State the blood parasite species.
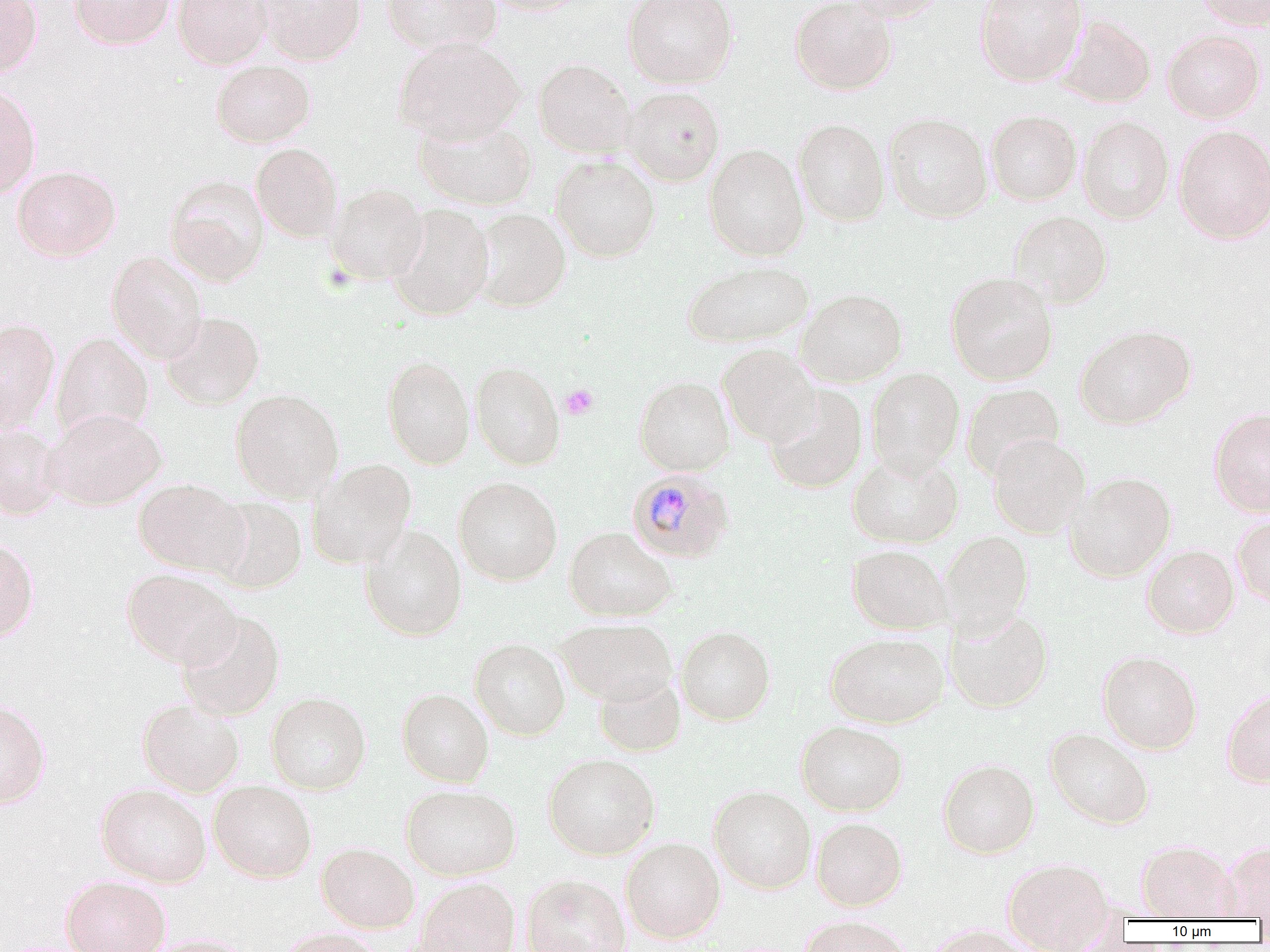
Plasmodium malariae.

Summary:
  - Coordinate format: approximate bounding boxes as [x1, y1, x2, y2] in pixels
  - Plasmodium malariae-infected red blood cell locations: [626, 469, 735, 564]
  - Platelet locations: [560, 384, 599, 419]
  - Uninfected red blood cell locations: [0, 0, 42, 79], [70, 0, 175, 49], [172, 0, 272, 69], [258, 0, 366, 64], [382, 0, 501, 55], [480, 0, 590, 15], [623, 0, 738, 88], [790, 0, 897, 94], [844, 0, 949, 22], [974, 0, 1086, 85], [1195, 0, 1270, 30], [1056, 16, 1156, 107], [1163, 28, 1266, 122], [392, 38, 525, 142], [534, 58, 635, 157], [211, 60, 315, 147], [0, 84, 41, 198], [622, 86, 724, 186], [986, 110, 1082, 205], [884, 112, 992, 223], [1077, 116, 1174, 224], [413, 117, 538, 211], [793, 119, 890, 225], [1173, 125, 1270, 244], [250, 142, 344, 242], [704, 144, 808, 261], [550, 155, 661, 262], [12, 165, 120, 261], [164, 175, 270, 286], [326, 184, 428, 284], [386, 204, 494, 320], [472, 208, 571, 311], [1010, 210, 1112, 307], [107, 250, 207, 363], [682, 260, 814, 348], [946, 273, 1057, 385], [796, 288, 907, 387], [161, 311, 265, 409], [0, 317, 61, 431], [1076, 325, 1196, 428], [51, 332, 154, 439], [718, 344, 820, 446], [382, 354, 475, 469], [470, 360, 566, 470], [866, 367, 964, 477], [634, 375, 734, 475], [962, 383, 1064, 479], [764, 385, 868, 493], [231, 388, 344, 502], [1208, 407, 1270, 516], [45, 408, 166, 510], [0, 424, 65, 520], [988, 433, 1090, 537], [847, 451, 963, 549], [307, 458, 417, 569], [1065, 472, 1176, 581], [453, 477, 563, 586], [134, 479, 248, 575], [208, 496, 307, 594], [1233, 514, 1270, 608], [360, 525, 467, 641], [564, 526, 676, 621], [938, 531, 1033, 637], [0, 538, 40, 643], [847, 544, 952, 634], [1142, 545, 1238, 638], [121, 568, 240, 669], [945, 607, 1053, 713], [177, 609, 285, 721], [557, 618, 677, 705], [675, 625, 776, 725], [825, 632, 948, 728], [469, 638, 570, 740], [1097, 650, 1202, 754], [594, 673, 685, 756], [1221, 687, 1270, 787], [397, 688, 494, 786], [266, 691, 371, 794], [0, 699, 51, 809], [137, 700, 244, 797], [796, 720, 908, 815], [1045, 728, 1154, 829], [543, 753, 660, 860], [938, 758, 1039, 858], [209, 780, 317, 882], [96, 783, 211, 887], [401, 783, 521, 880], [709, 785, 816, 893], [811, 817, 907, 910], [621, 837, 725, 943], [1136, 840, 1238, 921], [1221, 841, 1270, 920], [316, 842, 420, 933], [1003, 857, 1114, 949], [521, 874, 631, 952], [61, 875, 171, 952], [414, 878, 521, 952], [797, 917, 913, 952], [922, 926, 1038, 951], [276, 928, 383, 952], [137, 933, 254, 952]
  - Field of view: single
  - Modality: optical microscopy
  - Magnification: 1000x
  - Image size: 1270×952 pixels
  - Preparation: thin blood smear